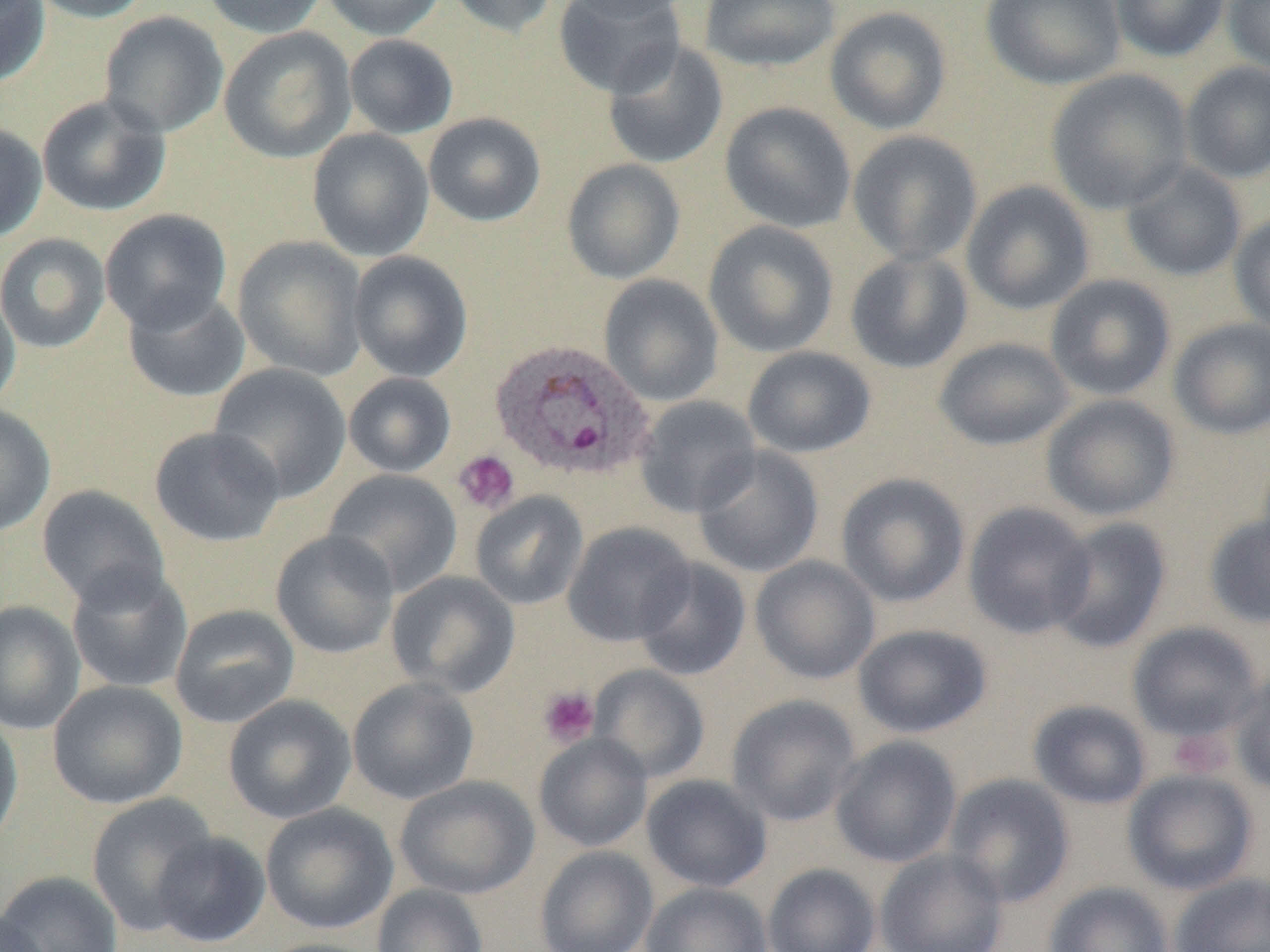
Summary:
  - Coordinate format: approximate bounding boxes as named x1/y1/x2/y2 corners in pixels
  - Uninfected red blood cell locations: (x1=0, y1=0, x2=50, y2=88), (x1=25, y1=0, x2=155, y2=23), (x1=200, y1=0, x2=328, y2=38), (x1=320, y1=0, x2=446, y2=41), (x1=445, y1=0, x2=561, y2=38), (x1=553, y1=0, x2=686, y2=98), (x1=559, y1=0, x2=692, y2=21), (x1=699, y1=0, x2=841, y2=73), (x1=981, y1=0, x2=1126, y2=90), (x1=1110, y1=0, x2=1231, y2=62), (x1=1223, y1=0, x2=1270, y2=76), (x1=824, y1=6, x2=952, y2=135), (x1=99, y1=11, x2=229, y2=139), (x1=219, y1=27, x2=357, y2=164), (x1=343, y1=34, x2=459, y2=139), (x1=602, y1=39, x2=728, y2=169), (x1=1180, y1=61, x2=1270, y2=184), (x1=1046, y1=68, x2=1194, y2=214), (x1=36, y1=94, x2=171, y2=217), (x1=719, y1=102, x2=856, y2=233), (x1=423, y1=113, x2=546, y2=227), (x1=0, y1=121, x2=48, y2=242), (x1=307, y1=128, x2=434, y2=262), (x1=847, y1=130, x2=983, y2=266), (x1=561, y1=158, x2=685, y2=284), (x1=1120, y1=161, x2=1247, y2=282), (x1=961, y1=180, x2=1095, y2=316), (x1=100, y1=209, x2=232, y2=333), (x1=1229, y1=211, x2=1270, y2=337), (x1=703, y1=220, x2=839, y2=358), (x1=0, y1=233, x2=111, y2=354), (x1=233, y1=236, x2=368, y2=382), (x1=844, y1=249, x2=974, y2=374), (x1=348, y1=250, x2=473, y2=381), (x1=598, y1=274, x2=724, y2=407), (x1=1045, y1=274, x2=1176, y2=401), (x1=0, y1=286, x2=21, y2=413), (x1=122, y1=287, x2=250, y2=403), (x1=1168, y1=318, x2=1270, y2=440), (x1=934, y1=337, x2=1075, y2=451), (x1=742, y1=346, x2=876, y2=458), (x1=208, y1=363, x2=352, y2=503), (x1=343, y1=372, x2=457, y2=478), (x1=1041, y1=394, x2=1181, y2=521), (x1=634, y1=395, x2=762, y2=518), (x1=0, y1=404, x2=56, y2=536), (x1=149, y1=426, x2=285, y2=547), (x1=692, y1=445, x2=824, y2=578), (x1=323, y1=469, x2=462, y2=597), (x1=836, y1=472, x2=971, y2=608), (x1=36, y1=485, x2=170, y2=609), (x1=470, y1=491, x2=589, y2=610), (x1=963, y1=501, x2=1095, y2=639), (x1=1203, y1=513, x2=1270, y2=629), (x1=1047, y1=516, x2=1173, y2=654), (x1=563, y1=521, x2=696, y2=647), (x1=271, y1=530, x2=400, y2=659), (x1=750, y1=555, x2=881, y2=685), (x1=633, y1=558, x2=752, y2=681), (x1=65, y1=564, x2=193, y2=694), (x1=386, y1=571, x2=521, y2=698), (x1=0, y1=601, x2=85, y2=735), (x1=169, y1=604, x2=300, y2=729), (x1=1127, y1=621, x2=1263, y2=742), (x1=853, y1=623, x2=993, y2=738), (x1=588, y1=664, x2=711, y2=783), (x1=1231, y1=668, x2=1270, y2=795), (x1=347, y1=677, x2=480, y2=805), (x1=47, y1=680, x2=188, y2=810), (x1=223, y1=694, x2=356, y2=823), (x1=726, y1=694, x2=861, y2=826), (x1=1028, y1=699, x2=1153, y2=810), (x1=0, y1=709, x2=23, y2=855), (x1=534, y1=733, x2=653, y2=852), (x1=830, y1=735, x2=962, y2=868), (x1=1123, y1=768, x2=1259, y2=896), (x1=944, y1=773, x2=1075, y2=908), (x1=641, y1=774, x2=772, y2=893), (x1=395, y1=775, x2=539, y2=899), (x1=86, y1=793, x2=218, y2=937), (x1=260, y1=803, x2=398, y2=935), (x1=151, y1=831, x2=271, y2=948), (x1=535, y1=846, x2=658, y2=952), (x1=875, y1=848, x2=1008, y2=952), (x1=763, y1=862, x2=881, y2=952), (x1=0, y1=871, x2=124, y2=952), (x1=1169, y1=872, x2=1270, y2=952), (x1=641, y1=882, x2=772, y2=952), (x1=1043, y1=882, x2=1174, y2=952), (x1=371, y1=884, x2=489, y2=952), (x1=0, y1=909, x2=49, y2=951), (x1=257, y1=937, x2=387, y2=952)
  - Plasmodium ovale-infected red blood cell locations: (x1=489, y1=338, x2=656, y2=482)
  - Platelet locations: (x1=453, y1=449, x2=520, y2=515), (x1=538, y1=685, x2=600, y2=747), (x1=1169, y1=728, x2=1233, y2=778)
  - Slide-level diagnosis: Plasmodium ovale
  - Image size: 1270×952 pixels
  - Preparation: thin blood film
  - Modality: light microscopy
  - Field of view: single
  - Magnification: 1000x